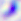
Photomicrograph. Toxoplasma gondii is seen. 400x magnification.